Locate the red blood cells and classify each one as Plasmodium falciparum-infected, uninfected, or of indeterminate infection status.
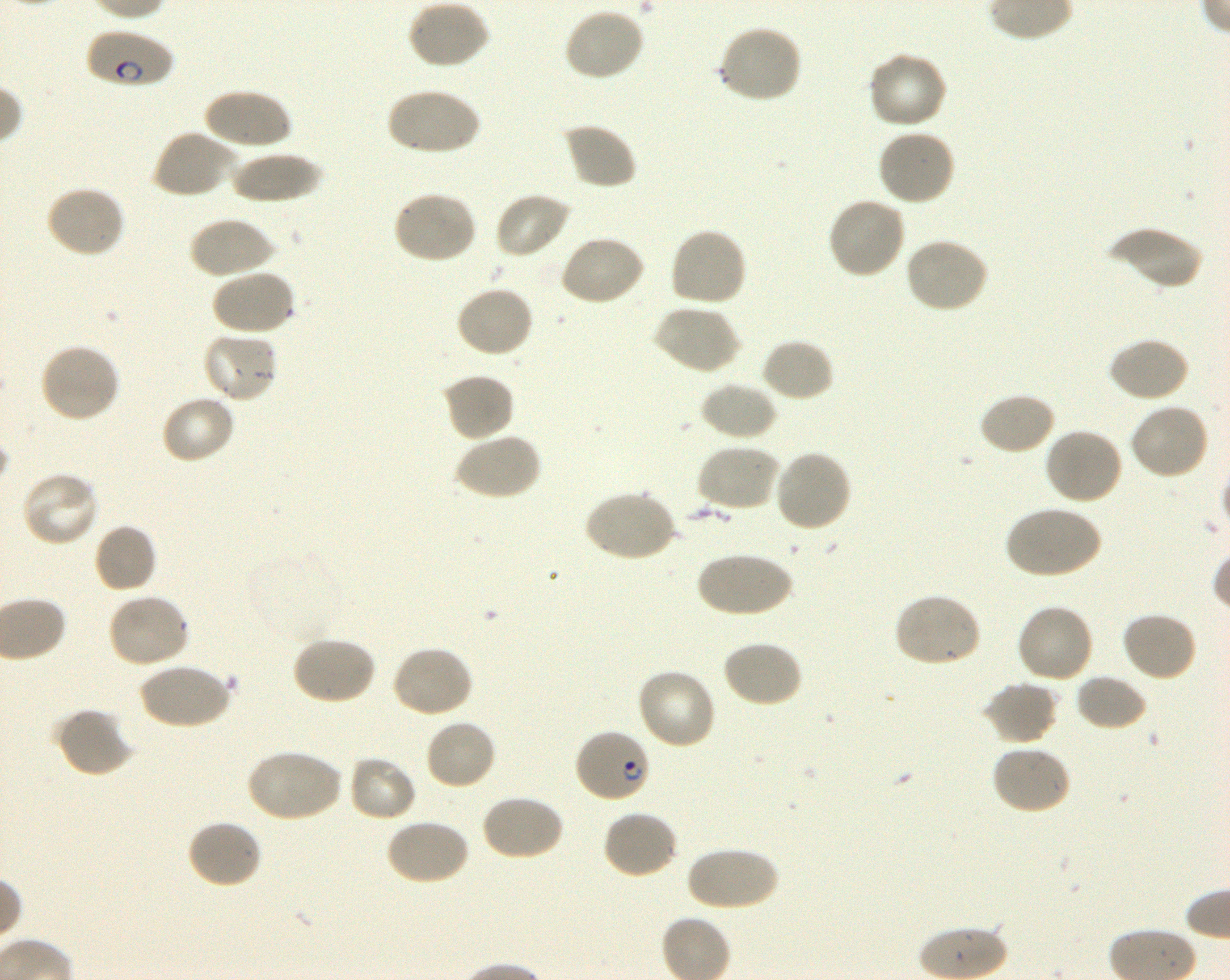
Approximate bounding rectangles given as corner coordinates in pixels from the top-left. Not every red blood cell is marked. A life-cycle stage — or a range of stages, where the recorded stages span more than one — follows each staged infected red blood cell.
Infected red blood cells: (x1=87, y1=27, x2=174, y2=89) early ring to early trophozoite; (x1=574, y1=728, x2=651, y2=804) ring.
Red blood cells of indeterminate infection status: (x1=246, y1=552, x2=340, y2=643).
Uninfected red blood cells: (x1=406, y1=0, x2=490, y2=70), (x1=562, y1=6, x2=645, y2=82), (x1=717, y1=23, x2=803, y2=103), (x1=866, y1=51, x2=948, y2=131), (x1=203, y1=87, x2=292, y2=152), (x1=386, y1=87, x2=480, y2=156), (x1=561, y1=122, x2=638, y2=191), (x1=151, y1=128, x2=237, y2=199), (x1=876, y1=129, x2=956, y2=207), (x1=229, y1=151, x2=325, y2=203), (x1=43, y1=185, x2=126, y2=259), (x1=391, y1=190, x2=477, y2=265), (x1=493, y1=192, x2=572, y2=259), (x1=826, y1=196, x2=907, y2=280), (x1=188, y1=215, x2=274, y2=279), (x1=1106, y1=225, x2=1203, y2=292), (x1=669, y1=227, x2=749, y2=308), (x1=558, y1=234, x2=646, y2=308), (x1=903, y1=237, x2=989, y2=314), (x1=209, y1=269, x2=296, y2=337), (x1=455, y1=285, x2=535, y2=358), (x1=653, y1=304, x2=741, y2=375), (x1=201, y1=331, x2=279, y2=404), (x1=1108, y1=336, x2=1190, y2=403), (x1=760, y1=338, x2=834, y2=402), (x1=38, y1=343, x2=122, y2=424), (x1=440, y1=372, x2=515, y2=443), (x1=700, y1=380, x2=779, y2=441), (x1=977, y1=392, x2=1057, y2=456), (x1=160, y1=394, x2=236, y2=465), (x1=1129, y1=402, x2=1211, y2=480), (x1=1043, y1=426, x2=1124, y2=505), (x1=454, y1=431, x2=542, y2=501), (x1=696, y1=444, x2=781, y2=513), (x1=773, y1=450, x2=852, y2=534), (x1=21, y1=470, x2=100, y2=548), (x1=583, y1=488, x2=676, y2=562), (x1=1005, y1=505, x2=1101, y2=579), (x1=93, y1=523, x2=158, y2=594), (x1=695, y1=552, x2=795, y2=617), (x1=107, y1=592, x2=192, y2=669), (x1=892, y1=592, x2=983, y2=668), (x1=1015, y1=602, x2=1095, y2=684), (x1=1120, y1=611, x2=1199, y2=683), (x1=291, y1=636, x2=377, y2=705), (x1=720, y1=639, x2=804, y2=708), (x1=391, y1=644, x2=475, y2=719), (x1=139, y1=662, x2=232, y2=730), (x1=636, y1=667, x2=718, y2=751), (x1=1075, y1=673, x2=1147, y2=731), (x1=981, y1=681, x2=1058, y2=745), (x1=55, y1=706, x2=136, y2=778), (x1=424, y1=718, x2=497, y2=791), (x1=991, y1=743, x2=1072, y2=815), (x1=245, y1=748, x2=342, y2=823), (x1=347, y1=756, x2=417, y2=823), (x1=480, y1=794, x2=565, y2=862), (x1=602, y1=809, x2=680, y2=881), (x1=385, y1=818, x2=470, y2=887), (x1=186, y1=819, x2=262, y2=890), (x1=686, y1=845, x2=779, y2=912).

objective = 100x, oil immersion, numerical aperture 1.30
culture = shaking in-vitro Plasmodium falciparum strain 3D7
field of view = single
donor blood group = O+
stain = Giemsa
preparation = thin blood smear
image size = 1230×980 pixels